State the blood parasite species.
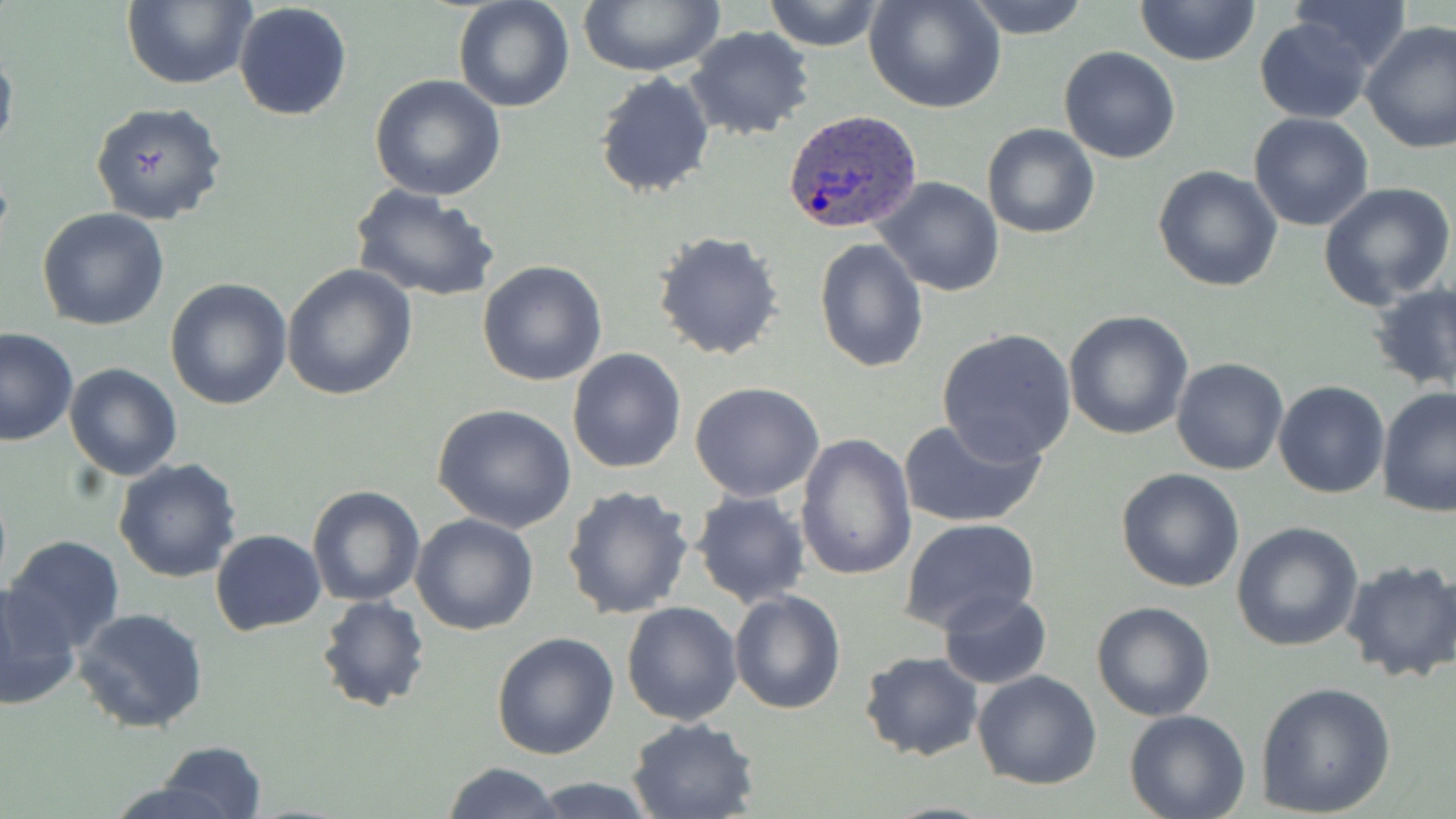

Plasmodium ovale.

{
  "magnification": "1000x",
  "modality": "light microscopy",
  "stain": "May-Grünwald-Giemsa",
  "plasmodium_ovale_infected_red_blood_cell_locations": "approximate bounding boxes as (x1, y1, x2, y2) in pixels: (783, 110, 924, 234)",
  "uninfected_red_blood_cell_locations": "approximate bounding boxes as (x1, y1, x2, y2) in pixels: (120, 0, 255, 89), (453, 0, 575, 113), (573, 0, 726, 76), (762, 0, 884, 51), (865, 0, 1006, 115), (962, 0, 1091, 40), (1134, 0, 1260, 68), (1288, 1, 1413, 70), (232, 2, 353, 122), (1256, 19, 1372, 122), (1360, 21, 1456, 154), (684, 26, 815, 141), (0, 41, 19, 165), (1059, 46, 1182, 164), (594, 71, 716, 200), (368, 75, 507, 201), (89, 101, 228, 225), (1247, 112, 1375, 232), (982, 122, 1101, 239), (1152, 164, 1284, 292), (873, 177, 1005, 296), (1318, 181, 1455, 307), (349, 185, 500, 304), (38, 208, 170, 331), (651, 230, 785, 361), (813, 237, 927, 373), (478, 261, 608, 386), (281, 263, 417, 400), (164, 276, 292, 410), (1367, 284, 1456, 393), (1063, 310, 1195, 442), (0, 327, 77, 446), (936, 327, 1077, 464), (567, 349, 687, 474), (1171, 357, 1288, 476), (64, 363, 182, 480), (1273, 380, 1391, 498), (689, 382, 823, 501), (1375, 386, 1456, 518), (434, 404, 577, 533), (898, 415, 1047, 530), (796, 433, 919, 583), (112, 457, 243, 583), (1116, 467, 1245, 592), (307, 483, 425, 607), (561, 483, 696, 619), (689, 490, 811, 609), (410, 512, 539, 635), (899, 518, 1041, 636), (1231, 521, 1364, 651), (211, 528, 326, 635), (3, 535, 126, 654), (1339, 558, 1456, 682), (1, 582, 81, 711), (937, 588, 1051, 690), (728, 590, 847, 715), (316, 594, 430, 712), (622, 600, 743, 725), (1091, 600, 1215, 721), (70, 606, 209, 735), (491, 630, 620, 760), (858, 651, 983, 761), (973, 669, 1103, 789), (1254, 680, 1398, 817), (1124, 709, 1252, 819), (626, 716, 761, 819), (155, 741, 268, 817), (443, 761, 562, 819), (526, 777, 661, 817), (99, 779, 242, 819)",
  "image_size": "1456×819 pixels",
  "preparation": "thin blood film",
  "field_of_view": "single"
}